Classify this cell by malaria status.
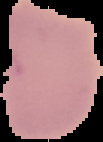

It is uninfected.

Segmented cell region on a black background. Image is 103×142 pixels. From a thin blood smear.